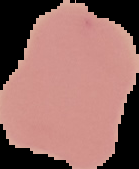
{
  "image_type": "segmented cell region on a black background",
  "image_size": "139×169 pixels",
  "preparation": "thin blood film",
  "result": "negative for Plasmodium parasites"
}